Name the parasite shown.
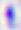
Toxoplasma gondii.

magnification = 400x
modality = photomicrograph